Give the position of every Plasmodium parasite.
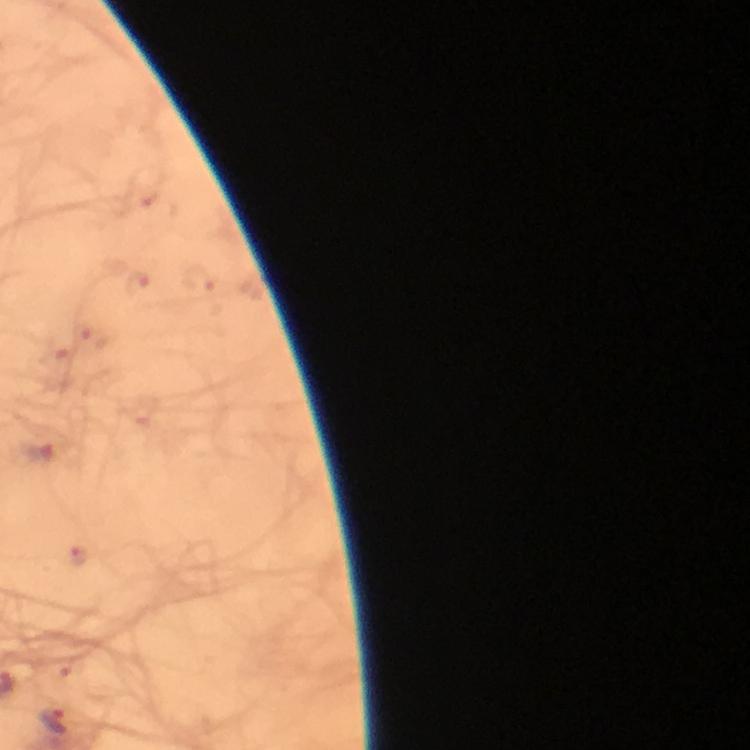

Approximate object centers, in pixels from the top-left corner.
Plasmodium parasites: (x=55, y=723).

capture: smartphone photograph through a microscope
preparation: thick blood smear
image_size: 750×750 pixels
cropped_from: one field of view
stain: Giemsa
context: from a malaria diagnostic workup
immersion_oil: applied
magnification: 100x